Point out malaria parasites and leukocytes.
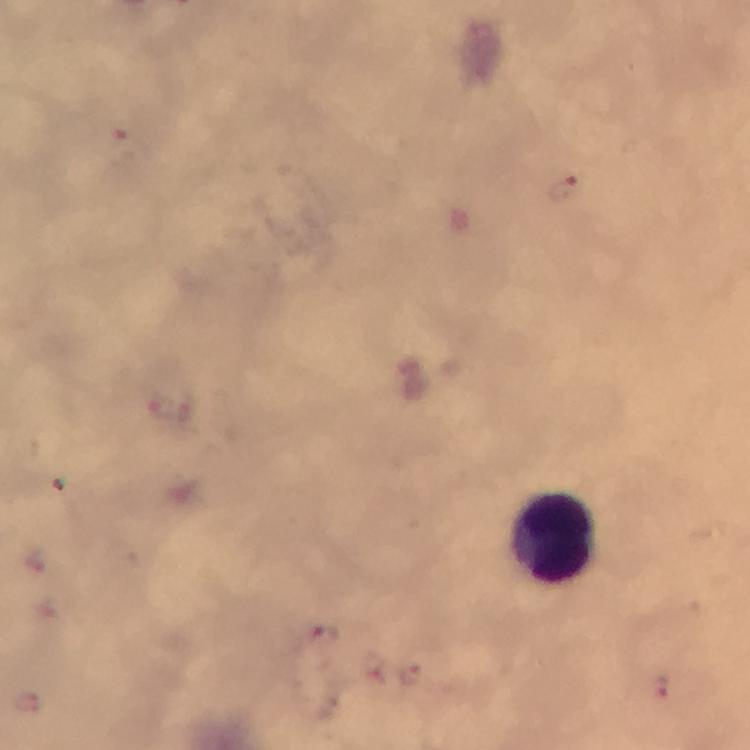

Approximate centers as {x, y} in pixels.
Malaria parasites: {130, 147}, {565, 190}, {324, 639}, {411, 673}, {661, 687}.
Leukocytes: {557, 537}.

Immersion oil was used. Thick smear. From a malaria diagnostic workup. 100x magnification. Photographed with a smartphone mounted on the microscope. Image is 750×750 pixels. Cropped region of a single field of view. Giemsa-stained preparation.